Point out each Plasmodium parasite.
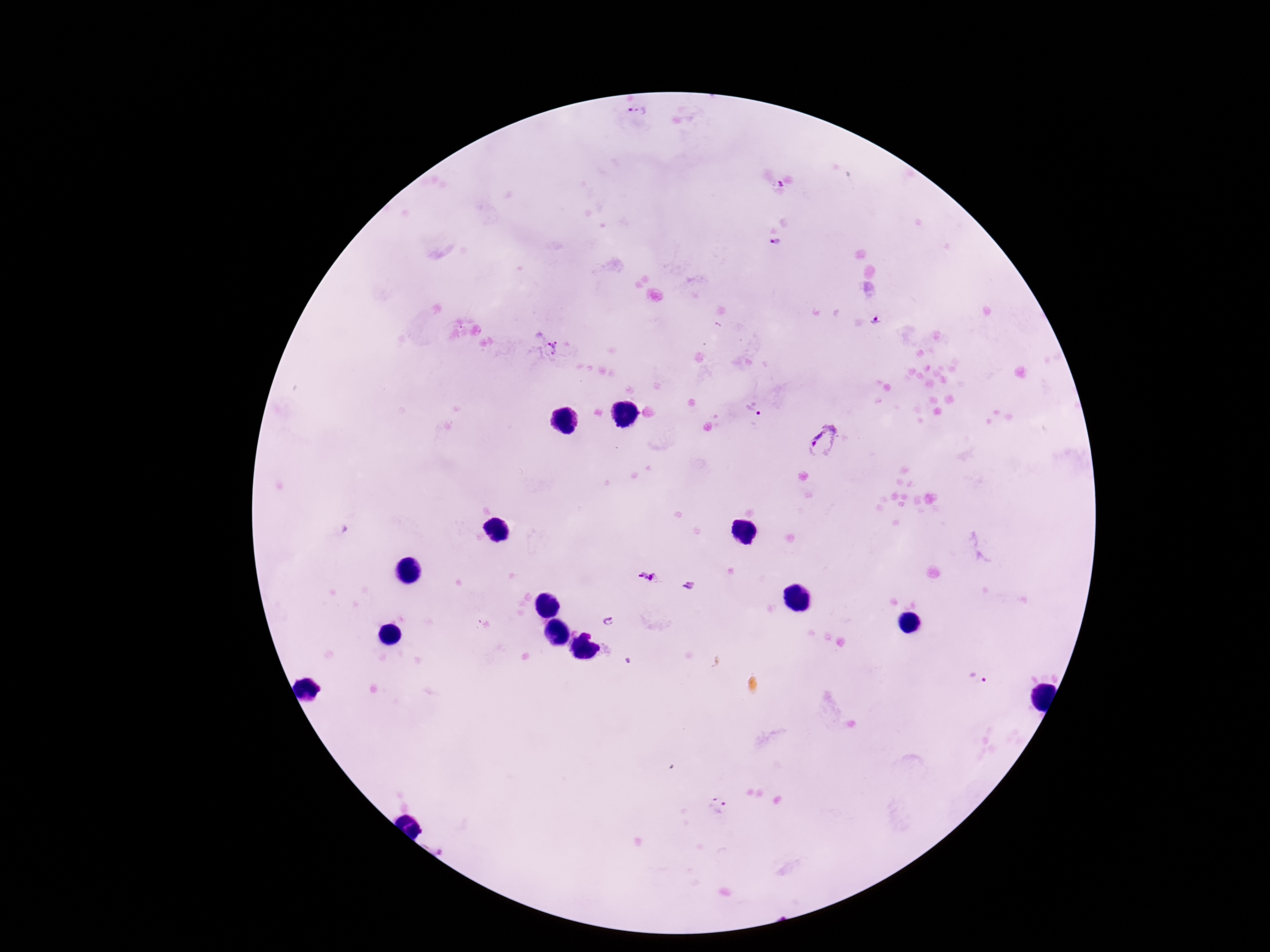

Approximate object centers, in pixels from the top-left corner.
Plasmodium parasites: (x=637, y=115), (x=778, y=189), (x=775, y=243), (x=876, y=322), (x=552, y=347), (x=752, y=410), (x=824, y=441), (x=648, y=577), (x=691, y=585), (x=609, y=623), (x=977, y=680), (x=716, y=807).

Summary:
  - Preparation: thick blood film
  - Magnification: 100x
  - Image size: 1270×952 pixels
  - Stain: Giemsa
  - Capture: smartphone camera through the microscope eyepiece
  - Field of view: one from this slide
  - Patient malaria status: infected